Outline every malaria parasite.
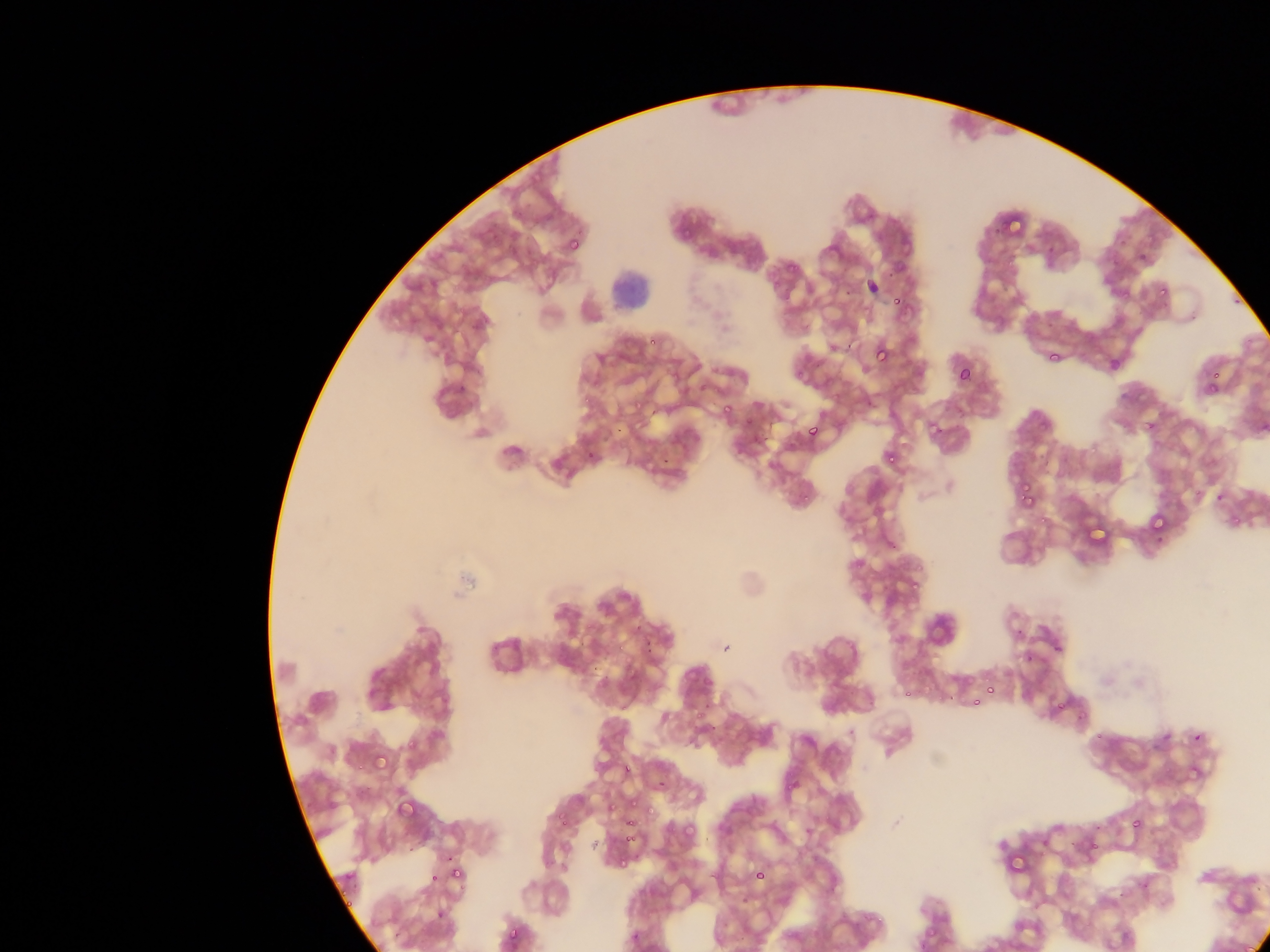
Approximate bounding boxes as {left, top, right, bottom} in pixels.
Malaria parasites: {682, 230, 691, 236}, {569, 238, 581, 251}, {1158, 290, 1166, 294}, {892, 298, 903, 305}, {876, 346, 889, 362}, {1048, 353, 1061, 362}, {958, 369, 972, 382}, {1208, 382, 1215, 392}, {724, 403, 731, 414}, {1145, 420, 1155, 430}, {808, 428, 818, 436}, {888, 455, 896, 463}, {662, 457, 670, 464}, {1021, 483, 1031, 492}, {804, 494, 810, 502}, {1017, 494, 1026, 501}, {1025, 496, 1036, 504}, {1151, 518, 1166, 531}, {914, 581, 921, 592}, {1028, 656, 1032, 664}, {986, 687, 996, 695}, {973, 697, 981, 708}, {1057, 700, 1068, 710}, {697, 709, 709, 717}, {1079, 712, 1087, 717}, {1194, 732, 1201, 740}, {408, 736, 416, 752}, {373, 754, 388, 771}, {626, 764, 631, 772}, {631, 801, 640, 807}, {398, 802, 414, 814}, {609, 804, 617, 811}, {647, 807, 655, 814}, {557, 814, 565, 821}, {1133, 819, 1140, 828}, {562, 820, 569, 829}, {625, 820, 636, 827}, {683, 822, 696, 833}, {630, 834, 639, 841}, {625, 837, 630, 845}, {447, 852, 454, 862}, {451, 867, 462, 878}, {756, 867, 765, 880}, {430, 870, 440, 883}, {338, 892, 349, 897}, {344, 898, 355, 908}, {437, 911, 445, 920}, {509, 925, 520, 943} | approximate {x, y} pixel centers of objects too small to bound: {891, 273}, {848, 293}, {1237, 303}, {652, 342}, {848, 345}, {800, 375}, {1215, 375}, {586, 400}, {653, 413}, {749, 421}, {618, 429}, {1220, 497}, {1042, 520}, {1160, 539}, {1019, 632}, {1058, 648}, {909, 694}, {952, 697}, {1101, 737}, {361, 767}, {791, 788}, {1096, 846}, {411, 850}, {624, 863}, {463, 886}, {880, 918}, {397, 932}.

field of view = single
leukocyte locations = approximate bounding boxes as {left, top, right, bottom} in pixels: {609, 265, 657, 312}
preparation = thin blood film
capture = mobile-phone photograph through a microscope
image size = 1270×952 pixels
country = Ghana